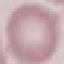

Summary:
  - Malaria status: uninfected
  - Capture: smartphone camera at the microscope eyepiece
  - Preparation: thin smear
  - Stain: Giemsa
  - Image type: cell patch, automatically extracted from a larger field of view and resized to 64 × 64 pixels